Give the extent of all Plasmodium vivax-infected red blood cells.
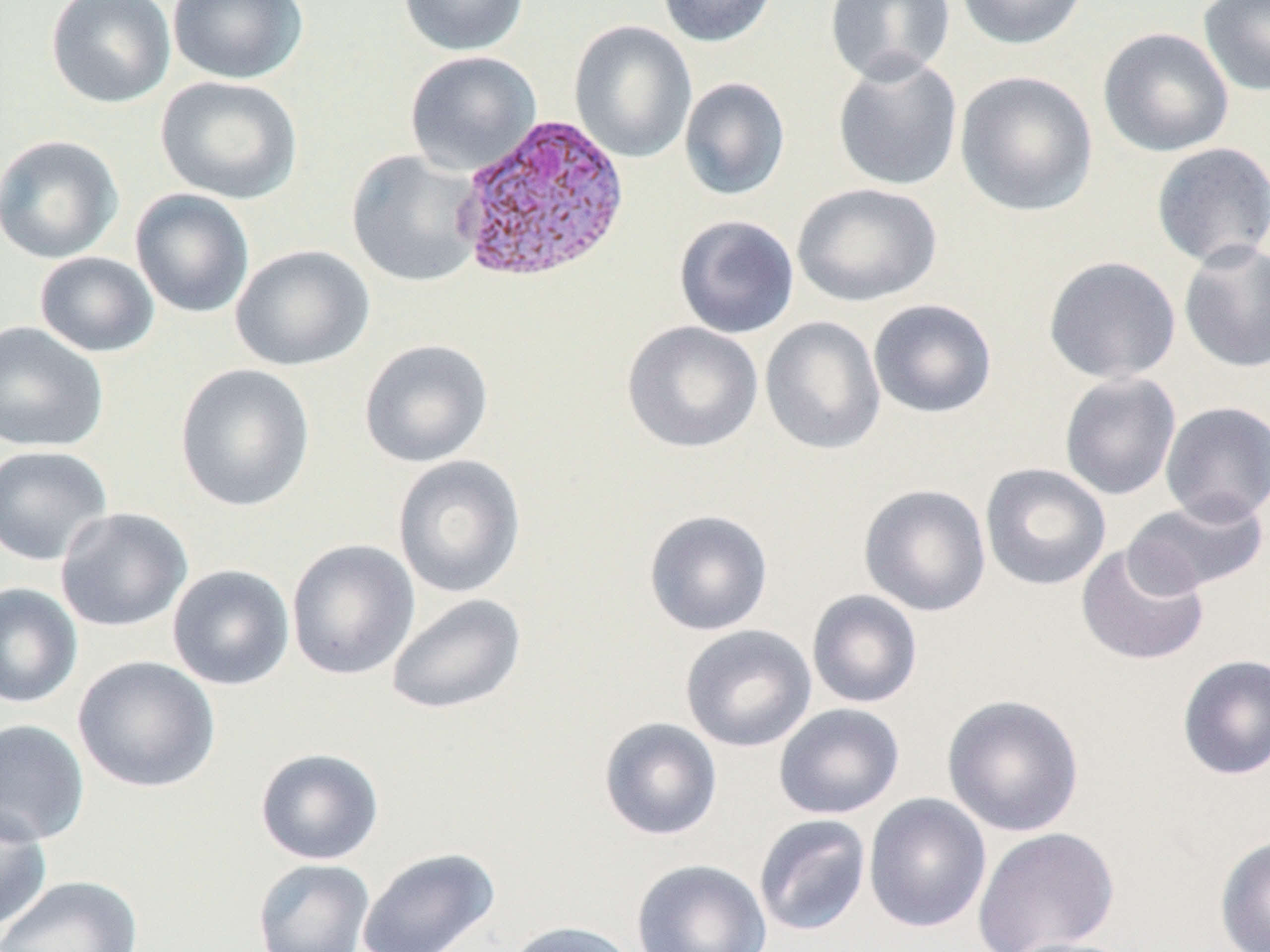

Approximate bounding boxes as (x1, y1, x2, y2) in pixels.
Plasmodium vivax-infected red blood cells: (452, 112, 632, 285).

Uninfected red blood cell locations: (46, 0, 176, 109), (167, 0, 308, 85), (398, 0, 529, 56), (657, 0, 778, 48), (825, 0, 956, 85), (955, 0, 1088, 50), (1198, 0, 1270, 96), (568, 20, 698, 163), (1097, 26, 1234, 158), (404, 50, 542, 176), (832, 54, 964, 192), (954, 70, 1098, 218), (155, 76, 302, 204), (678, 77, 791, 201), (0, 134, 123, 264), (1151, 142, 1270, 268), (346, 149, 485, 288), (792, 182, 942, 307), (130, 189, 255, 318), (673, 214, 799, 339), (1178, 240, 1270, 373), (231, 244, 375, 372), (34, 251, 160, 358), (1043, 256, 1181, 384), (868, 299, 997, 419), (760, 316, 886, 455), (0, 321, 109, 453), (622, 321, 764, 453), (359, 338, 494, 468), (174, 363, 315, 512), (1059, 372, 1181, 500), (1160, 401, 1270, 525), (0, 445, 113, 567), (392, 455, 526, 599), (980, 462, 1111, 591), (858, 483, 992, 617), (1123, 494, 1269, 597), (55, 507, 193, 633), (643, 509, 773, 636), (286, 538, 420, 680), (1076, 543, 1210, 666), (167, 564, 295, 690), (0, 582, 83, 708), (806, 589, 923, 709), (385, 593, 526, 715), (680, 624, 817, 752), (1177, 653, 1270, 780), (73, 655, 221, 794), (942, 693, 1085, 837), (773, 703, 905, 819), (598, 717, 723, 841), (0, 718, 90, 846), (255, 748, 384, 865), (863, 792, 991, 933), (0, 804, 52, 936), (753, 813, 872, 937), (971, 826, 1119, 952), (1214, 835, 1270, 952), (356, 847, 501, 952), (252, 858, 375, 952), (631, 859, 772, 952), (0, 875, 144, 952), (503, 920, 640, 952), (1000, 937, 1140, 952). Slide-level diagnosis: Plasmodium vivax. May-Grünwald-Giemsa stain. Thin blood smear. Captured at 1000x magnification. Optical microscopy. Image is 1270×952 pixels. Single field of view.